Report the malaria status of this cell.
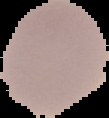

It is uninfected.

Summary:
  - Image size: 109×118 pixels
  - Preparation: thin blood smear
  - Image type: segmented cell region with the area outside set to black